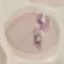
Malaria status: uninfected. Acquired by smartphone through the microscope eyepiece. Giemsa stain. Automatically extracted cell patch, resized to 64 × 64 pixels. Thin blood smear.